Outline each blood parasite and name the species.
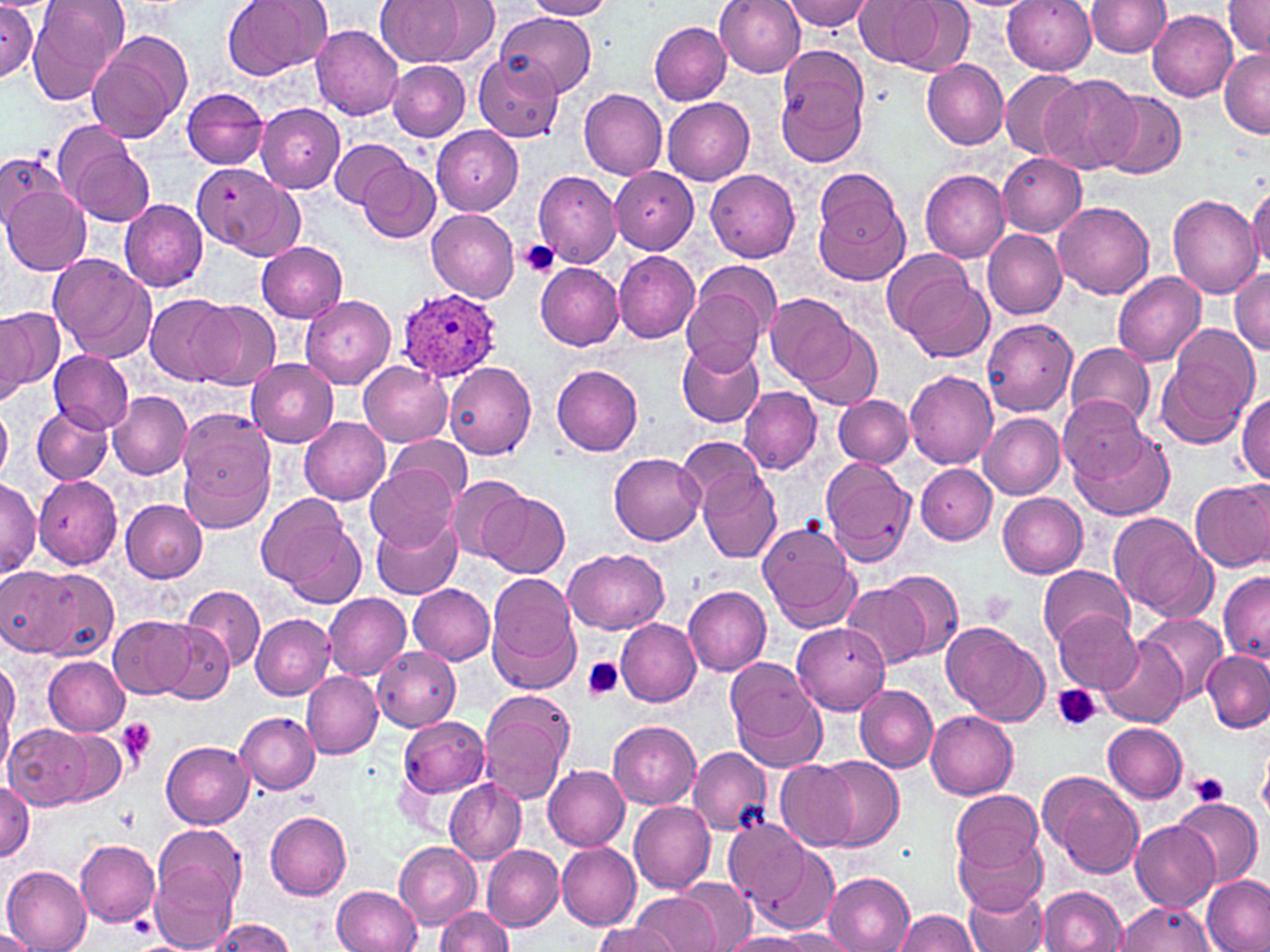

Approximate bounding boxes as [x1, y1, x2, y2] in pixels.
Plasmodium ovale-infected red blood cells: [393, 289, 501, 384].
No Plasmodium falciparum, Plasmodium malariae, Plasmodium vivax, Babesia divergens, or Trypanosoma brucei observed.

Uninfected red blood cell locations: [27, 0, 130, 105], [222, 0, 331, 81], [377, 0, 471, 66], [714, 0, 806, 77], [784, 0, 873, 31], [856, 0, 965, 71], [1002, 0, 1096, 74], [1224, 0, 1270, 55], [430, 1, 499, 64], [524, 1, 614, 20], [1087, 1, 1172, 57], [0, 4, 38, 79], [1148, 10, 1238, 101], [500, 12, 596, 96], [649, 22, 732, 104], [312, 25, 404, 120], [84, 30, 188, 143], [1219, 48, 1270, 137], [776, 50, 869, 166], [472, 53, 562, 142], [921, 58, 1009, 150], [387, 60, 469, 141], [998, 70, 1084, 160], [1040, 73, 1141, 175], [183, 88, 269, 168], [579, 89, 667, 178], [1101, 91, 1186, 180], [662, 95, 754, 185], [256, 104, 344, 193], [432, 125, 524, 215], [64, 137, 154, 227], [329, 137, 410, 209], [996, 152, 1085, 238], [0, 153, 56, 232], [360, 160, 442, 244], [202, 167, 307, 262], [610, 167, 698, 254], [705, 169, 801, 262], [533, 170, 622, 266], [919, 170, 1010, 261], [2, 184, 90, 274], [1247, 184, 1270, 272], [815, 185, 909, 285], [1166, 194, 1260, 299], [120, 199, 209, 291], [1054, 199, 1154, 298], [427, 208, 519, 302], [983, 230, 1066, 319], [256, 242, 348, 322], [882, 247, 975, 336], [614, 250, 701, 343], [47, 254, 157, 360], [536, 263, 623, 350], [1231, 267, 1270, 354], [901, 271, 993, 361], [1112, 271, 1206, 366], [680, 283, 771, 376], [144, 294, 237, 385], [766, 294, 857, 386], [299, 295, 396, 389], [191, 299, 279, 388], [0, 307, 57, 398], [982, 319, 1076, 416], [801, 324, 881, 409], [1158, 333, 1258, 446], [676, 339, 764, 428], [1066, 342, 1155, 429], [50, 350, 133, 432], [247, 359, 338, 447], [359, 361, 451, 447], [444, 362, 536, 459], [551, 365, 643, 456], [903, 370, 998, 468], [739, 387, 821, 474], [109, 391, 192, 478], [1236, 393, 1269, 482], [834, 395, 912, 468], [1056, 395, 1149, 479], [1, 403, 12, 483], [32, 405, 112, 483], [177, 410, 277, 529], [978, 412, 1065, 498], [298, 417, 389, 504], [1073, 429, 1173, 522], [387, 434, 471, 504], [677, 439, 769, 516], [610, 452, 705, 545], [820, 456, 916, 567], [916, 464, 997, 544], [365, 466, 458, 551], [698, 468, 782, 562], [448, 475, 527, 561], [34, 476, 121, 569], [1190, 480, 1270, 571], [0, 481, 40, 577], [482, 492, 569, 577], [998, 494, 1088, 577], [258, 496, 363, 604], [121, 499, 207, 582], [1108, 511, 1216, 622], [371, 514, 463, 599], [758, 522, 860, 632], [563, 547, 667, 635], [1038, 564, 1133, 647], [4, 565, 105, 658], [878, 569, 963, 661], [1218, 570, 1270, 664], [486, 576, 581, 695], [408, 583, 496, 665], [183, 585, 264, 670], [840, 585, 931, 669], [684, 586, 770, 675], [324, 593, 412, 679], [1054, 609, 1143, 692], [1138, 610, 1228, 703], [251, 614, 335, 699], [110, 615, 197, 700], [614, 617, 702, 707], [154, 621, 238, 704], [940, 621, 1049, 726], [791, 624, 891, 713], [1100, 641, 1187, 726], [374, 646, 460, 731], [1202, 651, 1269, 732], [42, 655, 131, 736], [0, 656, 20, 769], [726, 657, 823, 759], [300, 672, 383, 759], [853, 682, 938, 772], [479, 692, 575, 804], [927, 711, 1018, 799], [237, 712, 320, 794], [398, 716, 488, 797], [609, 721, 699, 808], [1104, 722, 1188, 804], [5, 724, 103, 810], [44, 729, 129, 806], [161, 741, 254, 829], [1260, 744, 1270, 821], [687, 747, 773, 835], [817, 755, 903, 851], [775, 760, 858, 850], [543, 765, 629, 850], [1040, 771, 1143, 877], [445, 776, 526, 864], [0, 778, 35, 862], [951, 789, 1042, 874], [1173, 797, 1262, 887], [629, 801, 716, 894], [264, 808, 351, 900], [725, 820, 810, 912], [1130, 820, 1219, 912], [953, 833, 1046, 913], [76, 839, 160, 924], [556, 841, 641, 929], [396, 842, 480, 928], [482, 845, 563, 931], [751, 845, 838, 934], [150, 849, 242, 952], [1, 866, 91, 951], [824, 872, 915, 952], [1201, 876, 1268, 952], [672, 878, 758, 948], [332, 885, 421, 952], [964, 885, 1048, 952], [1039, 885, 1127, 952], [629, 893, 720, 952], [1115, 901, 1216, 951], [434, 907, 511, 952], [893, 909, 978, 952], [207, 919, 294, 952], [597, 919, 674, 952], [0, 929, 39, 951], [772, 929, 857, 950], [723, 933, 815, 951]. Platelet locations: [518, 240, 562, 277], [978, 590, 1014, 625], [581, 658, 624, 701], [1052, 684, 1101, 733], [114, 718, 158, 767], [1190, 771, 1230, 805]. Slide-level diagnosis: Plasmodium ovale. Optical microscopy. May-Grünwald-Giemsa-stained preparation. Thin blood smear. Single field of view. Image is 1270×952 pixels. Captured at 1000x magnification.